Name the blood parasite species.
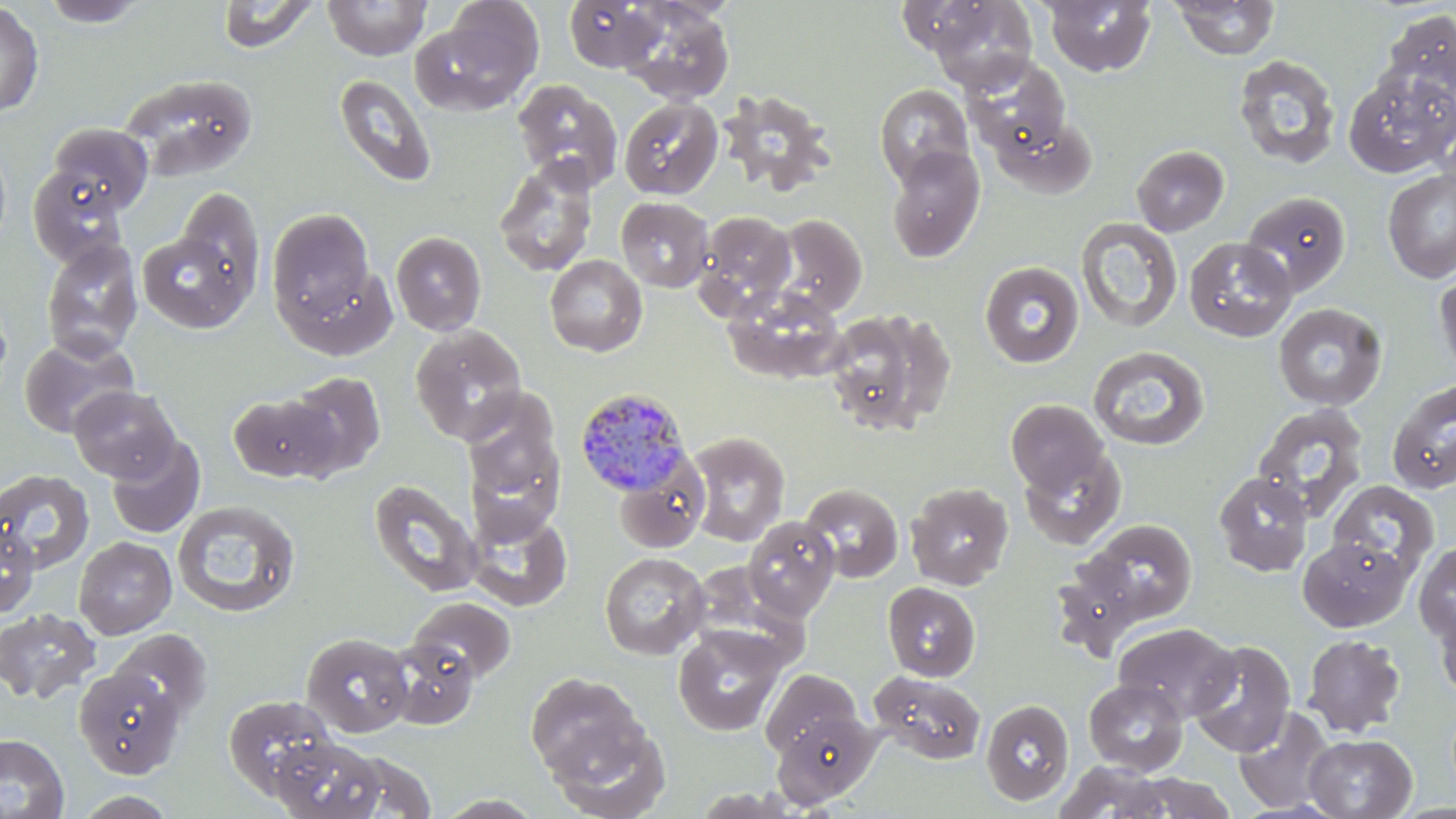
Plasmodium malariae.

{
  "preparation": "thin blood smear",
  "modality": "light microscopy",
  "plasmodium_malariae_infected_red_blood_cell_locations": "approximate bounding boxes as named x1/y1/x2/y2 corners in pixels: (x1=574, y1=387, x2=693, y2=495)",
  "magnification": "1000x",
  "field_of_view": "single",
  "stain": "May-Grünwald-Giemsa",
  "uninfected_red_blood_cell_locations": "approximate bounding boxes as named x1/y1/x2/y2 corners in pixels: (x1=35, y1=0, x2=152, y2=28), (x1=324, y1=0, x2=430, y2=60), (x1=564, y1=0, x2=662, y2=72), (x1=618, y1=0, x2=734, y2=105), (x1=1169, y1=0, x2=1279, y2=60), (x1=0, y1=1, x2=44, y2=117), (x1=216, y1=1, x2=319, y2=54), (x1=922, y1=1, x2=1037, y2=93), (x1=1043, y1=1, x2=1156, y2=77), (x1=411, y1=9, x2=542, y2=114), (x1=1381, y1=9, x2=1456, y2=109), (x1=963, y1=53, x2=1071, y2=155), (x1=1233, y1=54, x2=1341, y2=171), (x1=1344, y1=69, x2=1456, y2=177), (x1=119, y1=73, x2=258, y2=180), (x1=334, y1=73, x2=437, y2=188), (x1=511, y1=78, x2=623, y2=191), (x1=874, y1=84, x2=974, y2=187), (x1=720, y1=90, x2=834, y2=196), (x1=619, y1=97, x2=723, y2=199), (x1=992, y1=115, x2=1096, y2=198), (x1=48, y1=121, x2=154, y2=214), (x1=0, y1=139, x2=11, y2=251), (x1=1131, y1=144, x2=1229, y2=236), (x1=886, y1=145, x2=985, y2=263), (x1=494, y1=156, x2=599, y2=278), (x1=27, y1=165, x2=128, y2=268), (x1=1382, y1=168, x2=1456, y2=284), (x1=175, y1=186, x2=266, y2=305), (x1=1240, y1=191, x2=1351, y2=297), (x1=616, y1=197, x2=714, y2=292), (x1=267, y1=207, x2=376, y2=330), (x1=693, y1=211, x2=796, y2=318), (x1=769, y1=214, x2=868, y2=319), (x1=1076, y1=217, x2=1182, y2=333), (x1=138, y1=230, x2=252, y2=333), (x1=390, y1=231, x2=487, y2=336), (x1=1184, y1=236, x2=1297, y2=342), (x1=40, y1=238, x2=144, y2=361), (x1=544, y1=254, x2=648, y2=356), (x1=979, y1=261, x2=1084, y2=369), (x1=284, y1=263, x2=398, y2=361), (x1=1433, y1=267, x2=1456, y2=384), (x1=723, y1=286, x2=848, y2=384), (x1=1273, y1=302, x2=1387, y2=411), (x1=823, y1=309, x2=956, y2=436), (x1=410, y1=325, x2=527, y2=444), (x1=18, y1=333, x2=140, y2=439), (x1=1088, y1=345, x2=1210, y2=450), (x1=284, y1=371, x2=386, y2=479), (x1=1388, y1=379, x2=1456, y2=494), (x1=69, y1=385, x2=180, y2=482), (x1=461, y1=387, x2=566, y2=532), (x1=228, y1=392, x2=340, y2=483), (x1=1006, y1=399, x2=1110, y2=497), (x1=1252, y1=403, x2=1370, y2=523), (x1=685, y1=431, x2=790, y2=546), (x1=105, y1=434, x2=205, y2=539), (x1=1018, y1=445, x2=1127, y2=550), (x1=614, y1=459, x2=710, y2=554), (x1=0, y1=469, x2=94, y2=575), (x1=1213, y1=471, x2=1313, y2=576), (x1=369, y1=480, x2=482, y2=597), (x1=1328, y1=480, x2=1440, y2=581), (x1=905, y1=481, x2=1014, y2=590), (x1=800, y1=483, x2=903, y2=583), (x1=172, y1=501, x2=301, y2=618), (x1=467, y1=506, x2=571, y2=612), (x1=743, y1=516, x2=840, y2=620), (x1=1082, y1=518, x2=1198, y2=625), (x1=0, y1=520, x2=39, y2=618), (x1=74, y1=536, x2=177, y2=640), (x1=1298, y1=536, x2=1411, y2=631), (x1=1413, y1=542, x2=1456, y2=644), (x1=599, y1=552, x2=709, y2=659), (x1=1050, y1=558, x2=1153, y2=659), (x1=882, y1=581, x2=981, y2=681), (x1=408, y1=596, x2=516, y2=684), (x1=1433, y1=598, x2=1456, y2=705), (x1=0, y1=608, x2=101, y2=704), (x1=1113, y1=623, x2=1239, y2=721), (x1=673, y1=626, x2=787, y2=735), (x1=110, y1=629, x2=212, y2=722), (x1=300, y1=632, x2=413, y2=738), (x1=1302, y1=633, x2=1405, y2=738), (x1=385, y1=638, x2=479, y2=729), (x1=1187, y1=640, x2=1296, y2=757), (x1=74, y1=667, x2=185, y2=778), (x1=760, y1=668, x2=863, y2=760), (x1=868, y1=669, x2=987, y2=764), (x1=526, y1=673, x2=646, y2=780), (x1=1083, y1=678, x2=1189, y2=775), (x1=223, y1=694, x2=338, y2=799), (x1=980, y1=699, x2=1075, y2=806), (x1=1233, y1=706, x2=1337, y2=813), (x1=773, y1=711, x2=880, y2=808), (x1=546, y1=716, x2=671, y2=819), (x1=0, y1=733, x2=69, y2=819), (x1=1303, y1=734, x2=1417, y2=818), (x1=269, y1=736, x2=387, y2=819), (x1=327, y1=750, x2=437, y2=819), (x1=1053, y1=761, x2=1172, y2=819), (x1=1120, y1=773, x2=1237, y2=818), (x1=69, y1=790, x2=181, y2=818), (x1=432, y1=793, x2=545, y2=818)",
  "image_size": "1456×819 pixels"
}